Locate and identify every blood parasite.
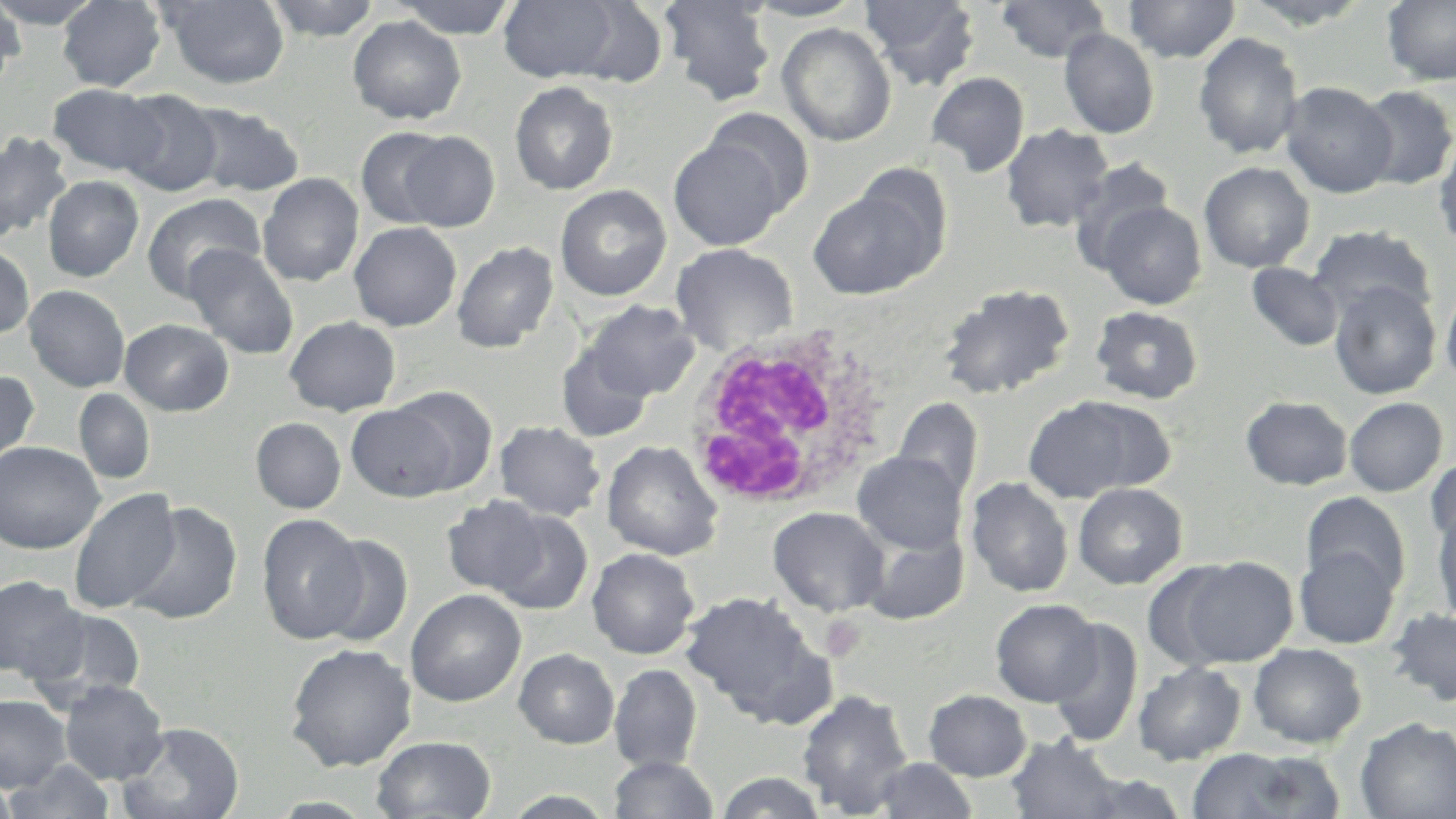
No blood parasites seen.

slide_level_diagnosis: negative for blood parasites
magnification: 1000x
white_blood_cell_locations: 'approximate bounding boxes as named x1/y1/x2/y2 corners in pixels: (x1=678, y1=327, x2=895, y2=514)'
preparation: thin blood film
uninfected_red_blood_cell_locations: 'approximate bounding boxes as named x1/y1/x2/y2 corners in pixels: (x1=0, y1=0, x2=23, y2=88), (x1=0, y1=0, x2=102, y2=29), (x1=57, y1=0, x2=166, y2=92), (x1=160, y1=0, x2=291, y2=89), (x1=264, y1=0, x2=383, y2=41), (x1=390, y1=0, x2=522, y2=39), (x1=499, y1=0, x2=621, y2=83), (x1=659, y1=0, x2=776, y2=106), (x1=743, y1=0, x2=866, y2=21), (x1=860, y1=0, x2=982, y2=91), (x1=996, y1=0, x2=1112, y2=63), (x1=1123, y1=0, x2=1241, y2=63), (x1=1239, y1=0, x2=1374, y2=29), (x1=1382, y1=0, x2=1456, y2=87), (x1=568, y1=2, x2=668, y2=86), (x1=347, y1=16, x2=466, y2=125), (x1=777, y1=24, x2=896, y2=146), (x1=1059, y1=29, x2=1159, y2=139), (x1=1193, y1=33, x2=1304, y2=160), (x1=926, y1=72, x2=1030, y2=177), (x1=510, y1=81, x2=618, y2=195), (x1=1280, y1=81, x2=1398, y2=198), (x1=47, y1=84, x2=166, y2=177), (x1=1355, y1=84, x2=1456, y2=190), (x1=115, y1=89, x2=224, y2=197), (x1=183, y1=101, x2=305, y2=197), (x1=703, y1=109, x2=815, y2=214), (x1=1001, y1=124, x2=1114, y2=233), (x1=355, y1=127, x2=456, y2=229), (x1=1433, y1=131, x2=1456, y2=249), (x1=0, y1=132, x2=73, y2=241), (x1=396, y1=132, x2=500, y2=231), (x1=668, y1=137, x2=788, y2=251), (x1=1069, y1=158, x2=1174, y2=270), (x1=852, y1=161, x2=955, y2=274), (x1=1199, y1=161, x2=1315, y2=273), (x1=258, y1=173, x2=364, y2=287), (x1=42, y1=175, x2=144, y2=282), (x1=555, y1=185, x2=671, y2=301), (x1=808, y1=189, x2=937, y2=299), (x1=141, y1=193, x2=265, y2=301), (x1=1096, y1=200, x2=1207, y2=309), (x1=349, y1=222, x2=462, y2=331), (x1=1308, y1=224, x2=1436, y2=324), (x1=452, y1=241, x2=559, y2=353), (x1=670, y1=243, x2=798, y2=355), (x1=0, y1=244, x2=35, y2=340), (x1=183, y1=244, x2=300, y2=360), (x1=1246, y1=263, x2=1344, y2=352), (x1=1440, y1=280, x2=1456, y2=391), (x1=1329, y1=281, x2=1442, y2=400), (x1=937, y1=283, x2=1075, y2=401), (x1=24, y1=285, x2=130, y2=392), (x1=583, y1=300, x2=700, y2=401), (x1=1090, y1=306, x2=1203, y2=405), (x1=284, y1=316, x2=401, y2=416), (x1=119, y1=318, x2=233, y2=416), (x1=556, y1=345, x2=654, y2=441), (x1=0, y1=369, x2=40, y2=471), (x1=389, y1=385, x2=498, y2=495), (x1=74, y1=388, x2=155, y2=485), (x1=1021, y1=395, x2=1164, y2=502), (x1=1240, y1=396, x2=1352, y2=490), (x1=893, y1=397, x2=983, y2=502), (x1=1343, y1=397, x2=1448, y2=497), (x1=346, y1=403, x2=458, y2=502), (x1=251, y1=417, x2=346, y2=513), (x1=494, y1=420, x2=606, y2=522), (x1=602, y1=440, x2=723, y2=561), (x1=0, y1=441, x2=104, y2=554), (x1=851, y1=451, x2=968, y2=554), (x1=1426, y1=453, x2=1456, y2=548), (x1=966, y1=478, x2=1073, y2=598), (x1=1073, y1=482, x2=1187, y2=590), (x1=68, y1=488, x2=181, y2=613), (x1=1301, y1=491, x2=1411, y2=598), (x1=441, y1=495, x2=550, y2=597), (x1=125, y1=502, x2=243, y2=625), (x1=1432, y1=506, x2=1456, y2=631), (x1=767, y1=507, x2=890, y2=617), (x1=489, y1=509, x2=593, y2=615), (x1=257, y1=513, x2=367, y2=644), (x1=859, y1=527, x2=968, y2=626), (x1=313, y1=534, x2=413, y2=646), (x1=1293, y1=543, x2=1401, y2=649), (x1=587, y1=547, x2=699, y2=660), (x1=1176, y1=556, x2=1298, y2=667), (x1=1141, y1=563, x2=1243, y2=672), (x1=0, y1=575, x2=86, y2=683), (x1=406, y1=590, x2=526, y2=706), (x1=681, y1=592, x2=826, y2=721), (x1=991, y1=598, x2=1102, y2=706), (x1=24, y1=606, x2=147, y2=708), (x1=1385, y1=607, x2=1456, y2=709), (x1=1049, y1=619, x2=1143, y2=747), (x1=285, y1=643, x2=417, y2=771), (x1=1248, y1=643, x2=1367, y2=748), (x1=514, y1=648, x2=619, y2=749), (x1=1132, y1=662, x2=1247, y2=765), (x1=609, y1=664, x2=702, y2=773), (x1=59, y1=680, x2=169, y2=784), (x1=796, y1=689, x2=914, y2=816), (x1=923, y1=689, x2=1032, y2=781), (x1=0, y1=695, x2=71, y2=790), (x1=1355, y1=717, x2=1456, y2=818), (x1=117, y1=722, x2=245, y2=819), (x1=1006, y1=734, x2=1124, y2=819), (x1=371, y1=735, x2=496, y2=818), (x1=1184, y1=748, x2=1344, y2=818), (x1=608, y1=755, x2=719, y2=818), (x1=872, y1=757, x2=979, y2=818), (x1=4, y1=759, x2=118, y2=819), (x1=713, y1=771, x2=831, y2=818), (x1=0, y1=774, x2=20, y2=819), (x1=500, y1=790, x2=619, y2=818)'
modality: light microscopy
stain: May-Grünwald-Giemsa
image_size: 1456×819 pixels
field_of_view: single